Give the position of each P. falciparum parasite with its life-cycle stage, each leukocyte, and any debris.
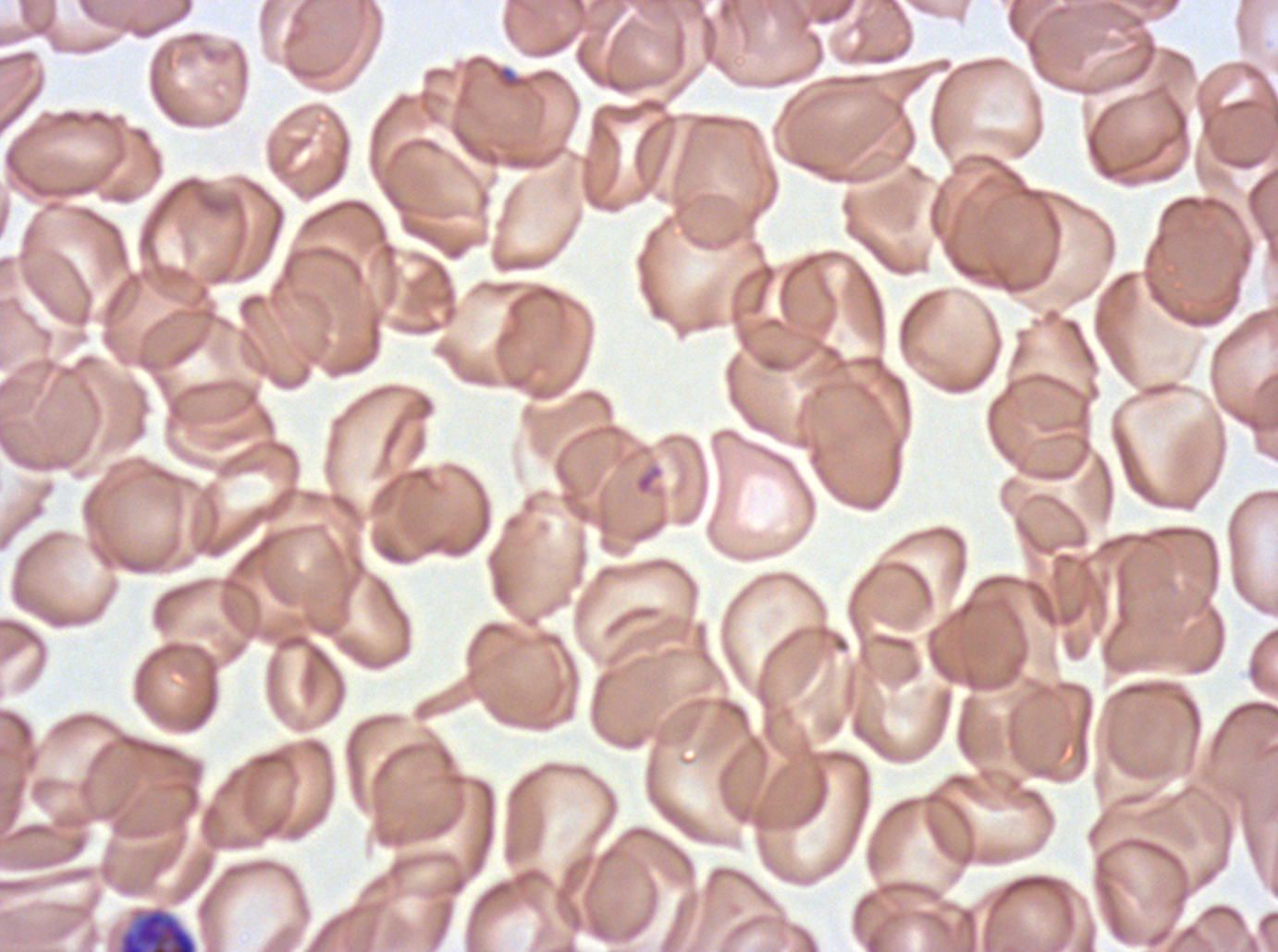
Approximate bounding rectangles given as corner coordinates in pixels from the top-left.
Late schizonts: (x1=117, y1=905, x2=199, y2=951).
Debris: (x1=498, y1=65, x2=520, y2=89).
No rings, late-ring/early-trophozoite forms, mid trophozoites, late trophozoites, early schizonts, segmenters, gametocytes, or leukocytes observed.

Ex-vivo P. falciparum culture from a patient in The Gambia, grown for 24 to 48 hours. Thin blood smear. Giemsa stain. One sub-image of a larger composite. Image is 1278×952 pixels.